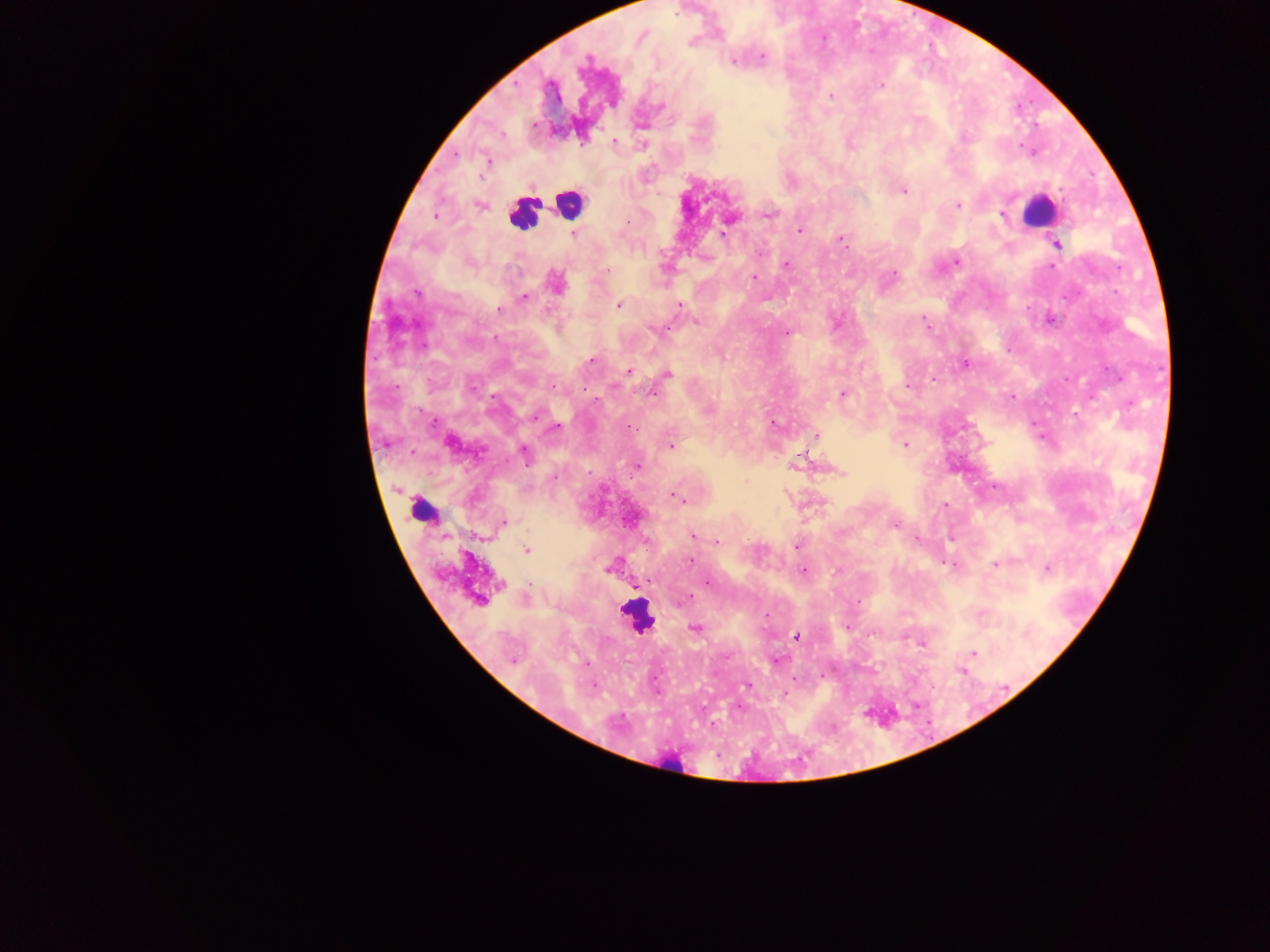
{
  "capture": "mobile-phone photograph through a microscope",
  "image_size": "1270×952 pixels",
  "malaria_parasite_locations": "approximate centers as x y in pixels: 762 57; 733 59; 881 85; 829 95; 614 141; 456 154; 487 161; 902 190; 958 204; 479 205; 769 214; 434 216; 1002 216; 730 217; 799 231; 573 233; 723 234; 840 238; 1057 244; 956 261; 785 265; 1051 266; 753 277; 555 282; 416 291; 523 298; 619 304; 678 305; 498 309; 1048 319; 697 321; 786 333; 590 360; 964 364; 629 371; 667 374; 933 379; 908 386; 652 392; 843 394; 1011 397; 596 400; 773 424; 553 429; 816 435; 449 441; 905 444; 671 446; 523 452; 796 462; 636 465; 840 472; 675 497; 946 505; 501 524; 894 524; 692 536; 916 538; 716 541; 796 547; 525 550; 691 560; 996 564; 612 565; 953 565; 1046 568; 803 571; 706 582; 636 584; 525 598; 687 598; 479 600; 857 600; 847 627; 695 629; 795 636; 922 643; 972 653; 513 659; 775 660; 966 666; 961 669; 748 685; 593 686; 784 694; 738 707",
  "preparation": "thick blood smear",
  "leukocyte_locations": "approximate centers as x y in pixels: 569 202; 1039 211; 524 213; 637 615",
  "field_of_view": "single",
  "object_labeled_both_malaria_parasite_and_leukocyte_by_the_source": "approximate centers as x y in pixels: 422 509",
  "country": "Ghana"
}